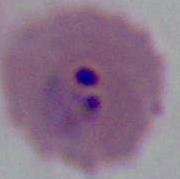

Summary:
  - Identification: Plasmodium
  - Modality: micrograph
  - Magnification: 400x or 1000x